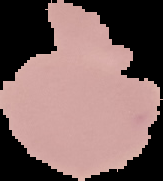
preparation = thin blood smear
image type = segmented cell region on a black background
malaria status = uninfected
image size = 163×181 pixels